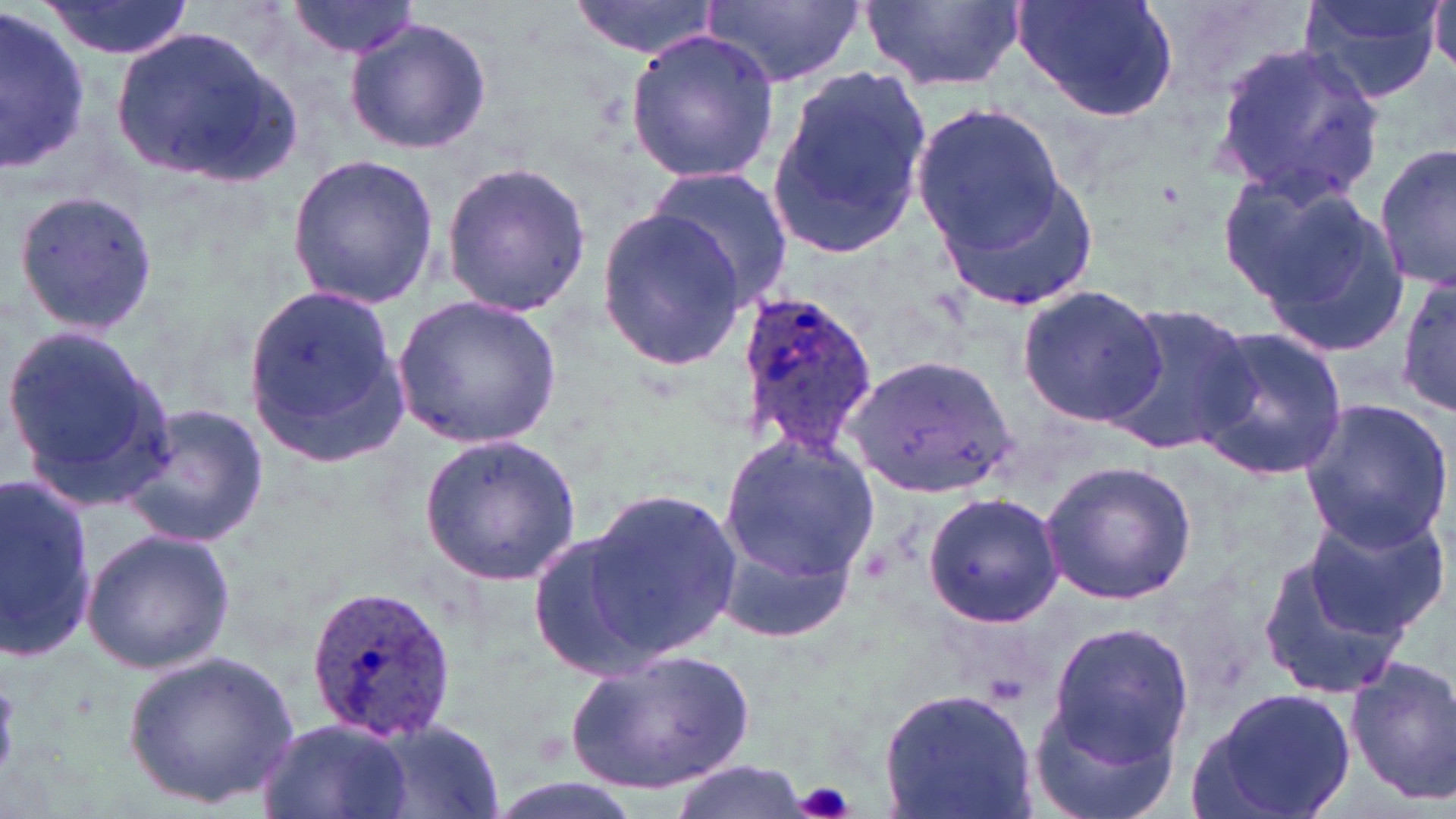
Approximate bounding boxes as (x1,y1)-(x2,y2) corner pairs in pixels. Plasmodium ovale-infected red blood cell locations: (730,284)-(881,468), (301,581)-(456,742). Uninfected red blood cell locations: (284,0)-(420,60), (568,0)-(722,61), (702,0)-(870,88), (857,0)-(1028,94), (1009,0)-(1182,123), (1293,0)-(1448,107), (1428,0)-(1456,77), (36,1)-(199,60), (0,8)-(92,173), (343,17)-(491,157), (111,20)-(304,189), (625,29)-(779,186), (1210,42)-(1385,205), (764,65)-(931,260), (912,100)-(1067,255), (1375,141)-(1456,290), (285,150)-(442,311), (438,159)-(594,317), (933,163)-(1101,315), (646,168)-(794,309), (1213,169)-(1376,313), (10,186)-(159,339), (1254,195)-(1417,359), (594,208)-(748,371), (1395,272)-(1454,419), (1017,284)-(1169,429), (240,288)-(411,459), (394,295)-(562,448), (1104,300)-(1255,460), (1,324)-(175,506), (1192,324)-(1348,484), (845,356)-(1018,495), (1299,399)-(1454,552), (118,404)-(270,548), (718,432)-(880,584), (421,433)-(582,585), (1040,459)-(1196,605), (0,471)-(98,662), (579,486)-(740,663), (922,492)-(1063,627), (1299,506)-(1449,642), (714,519)-(860,644), (524,527)-(665,680), (81,528)-(235,674), (1255,541)-(1418,700), (1045,622)-(1195,763), (123,647)-(302,809), (564,648)-(755,795), (1347,656)-(1456,806), (1194,685)-(1357,819), (880,686)-(1036,819), (1026,696)-(1182,819), (255,717)-(415,819), (366,719)-(506,818), (666,762)-(809,819). Platelet locations: (795,780)-(856,819). Slide-level diagnosis: Plasmodium ovale. Thin blood film. Captured at 1000x magnification. May-Grünwald-Giemsa-stained preparation. Image is 1456×819 pixels. Single field of view. Light microscopy.